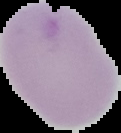

Image is 121×133 pixels. Segmented cell region on a black background. Result: negative for malaria parasites. From a thin blood film.